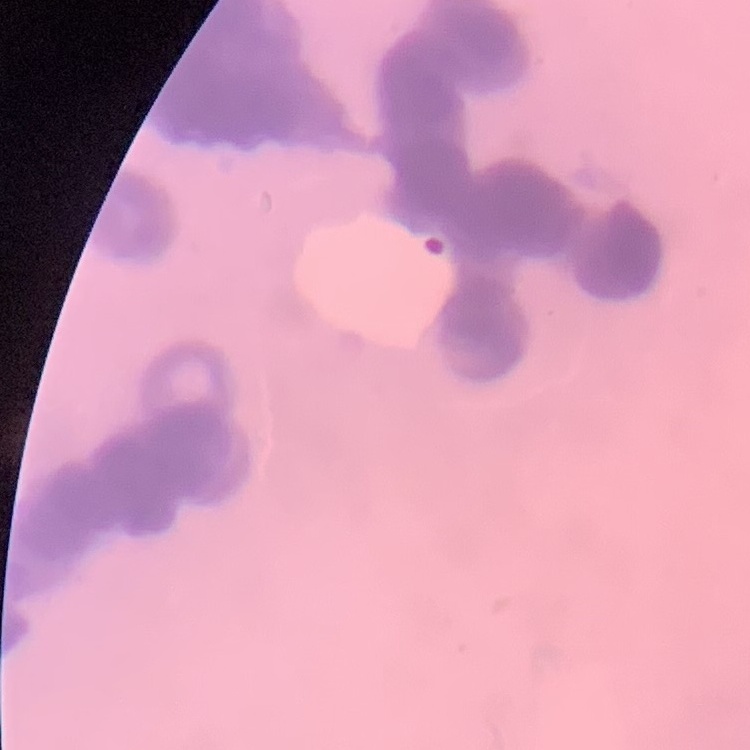
erythrocyte morphology = rouleaux formation
preparation = thin blood film
stain = Field's or Giemsa
image type = square crop of a larger photomicrograph